Locate and identify every blood parasite.
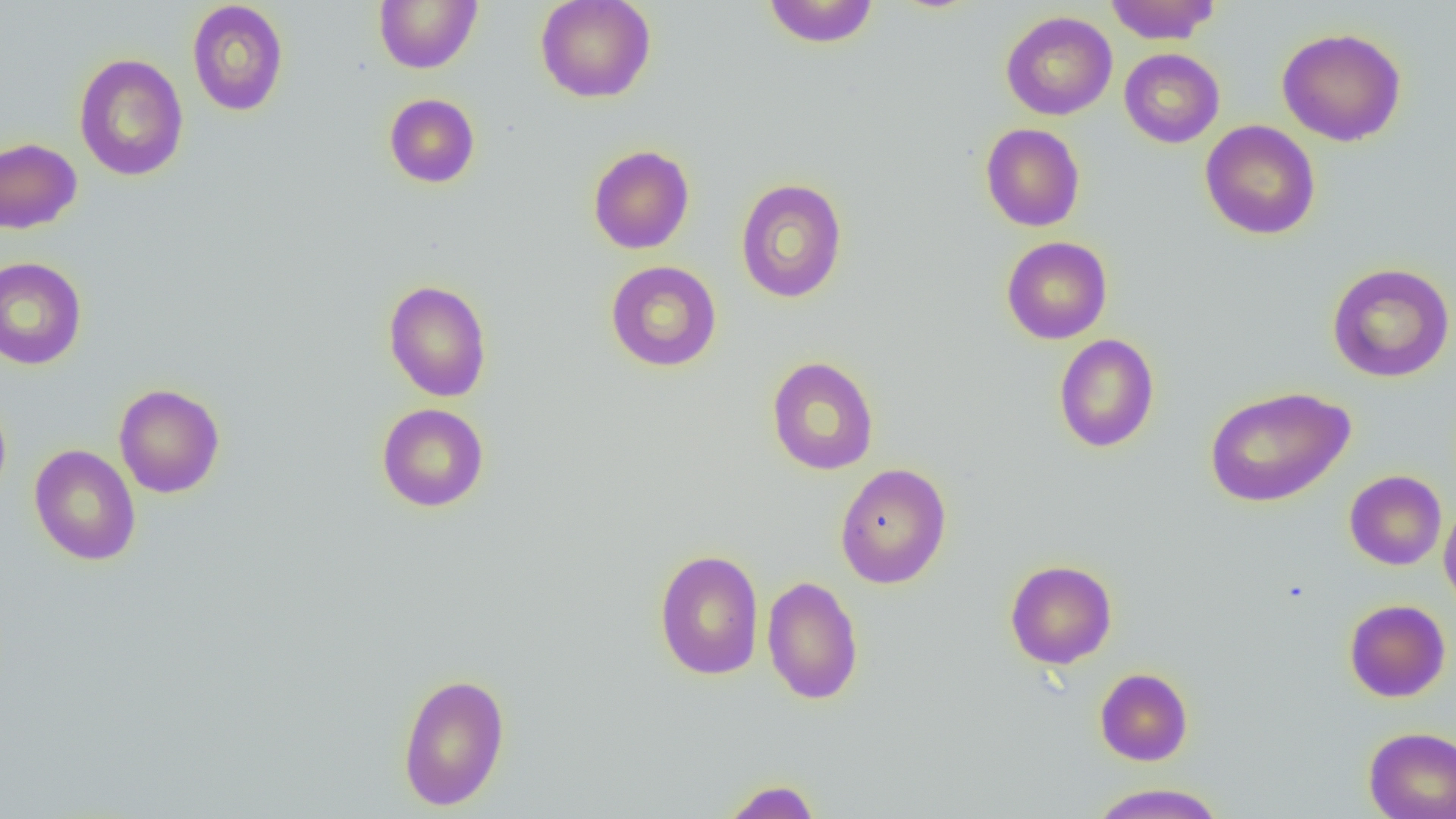

No blood parasites seen.

Approximate bounding boxes as [x1, y1, x2, y2] in pixels. Uninfected red blood cell locations: [374, 0, 482, 74], [535, 0, 656, 103], [1105, 0, 1220, 45], [187, 1, 289, 116], [762, 1, 880, 48], [1000, 11, 1117, 120], [1277, 27, 1407, 146], [1119, 48, 1224, 148], [74, 53, 188, 182], [384, 93, 480, 188], [1199, 120, 1321, 240], [980, 123, 1085, 232], [0, 137, 82, 234], [587, 144, 695, 254], [735, 178, 848, 303], [1001, 236, 1113, 344], [0, 257, 87, 370], [605, 260, 722, 372], [1327, 262, 1455, 382], [383, 279, 492, 402], [1053, 334, 1160, 453], [766, 356, 879, 475], [114, 383, 225, 498], [1205, 385, 1355, 508], [0, 394, 12, 504], [376, 403, 489, 512], [28, 444, 141, 566], [834, 462, 952, 589], [1344, 470, 1447, 570], [1439, 500, 1456, 614], [653, 549, 765, 680], [1004, 559, 1117, 669], [762, 575, 864, 705], [1343, 599, 1451, 702], [1095, 667, 1193, 766], [396, 672, 511, 811], [1363, 727, 1456, 819], [719, 778, 822, 819], [1087, 783, 1227, 819]. Slide-level diagnosis: no evidence of blood parasites. 1000x magnification. Image is 1456×819 pixels. Optical microscopy. Thin blood film. Single field of view.